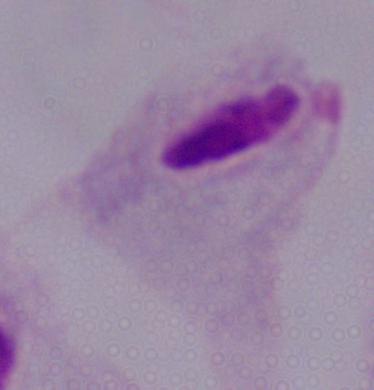
magnification: 1000x
identification: trichomonad
modality: micrograph